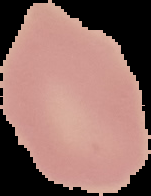

Summary:
  - Image size: 151×196 pixels
  - Preparation: thin blood film
  - Image type: cell region segmented out of the field of view; surrounding area masked to black
  - Result: negative for malaria parasites